Assess this cell for malaria.
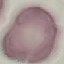

Uninfected.

Acquired by smartphone through the microscope eyepiece. Thin blood film. Giemsa-stained preparation. Cell patch, automatically extracted from a larger field of view and resized to 64 × 64 pixels.